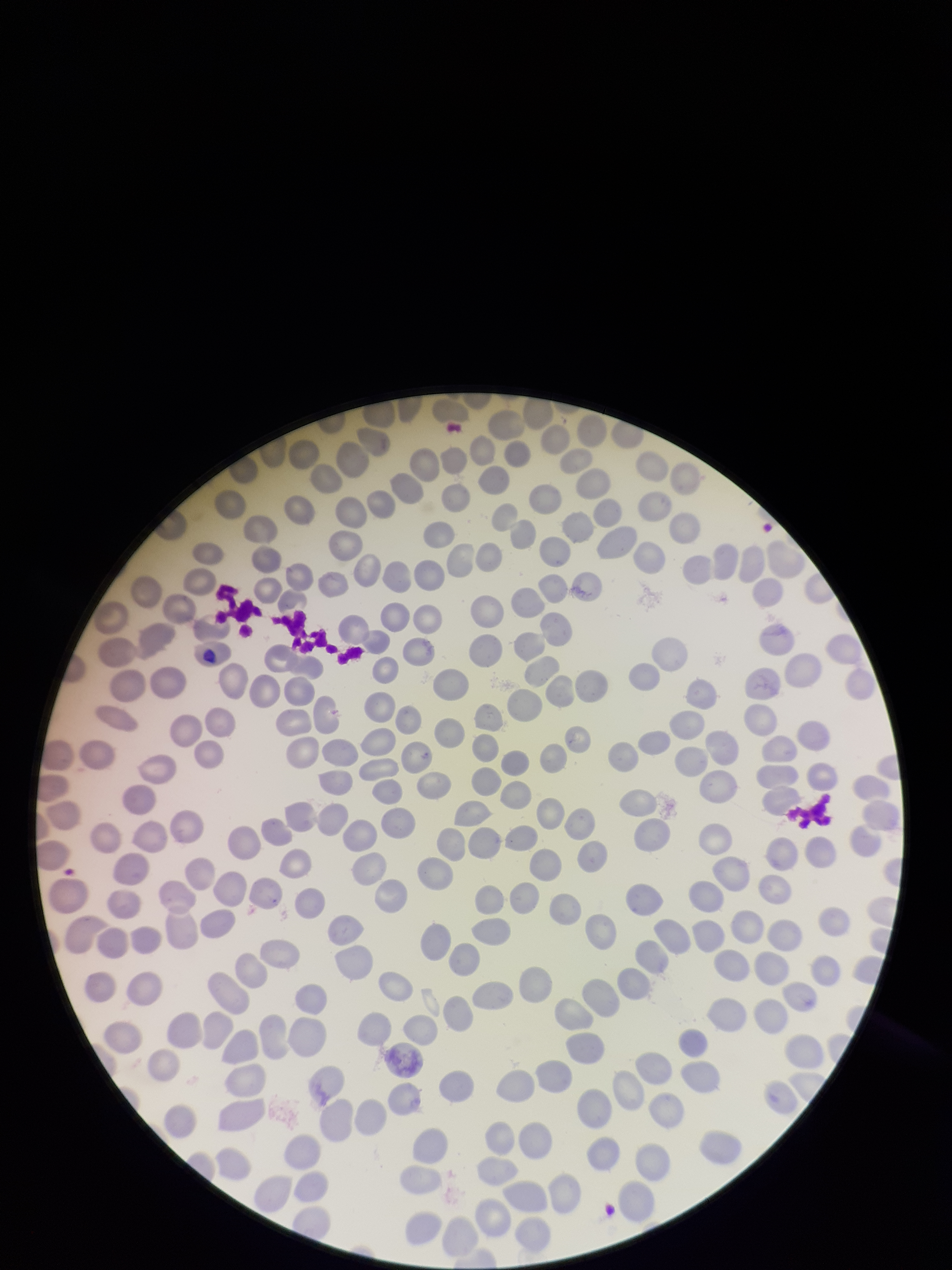
image size = 952×1270 pixels
capture = smartphone photograph through the microscope eyepiece
preparation = thin blood smear
red blood cell count = 265
patient malaria status = negative
field of view = single
stain = Giemsa
parasitized red blood cell count = 0
parasitized red blood cells = none identified